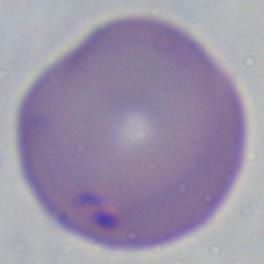

Summary:
  - Modality: micrograph
  - Identification: Babesia
  - Magnification: 1000x